Find the cells and give the type of each one.
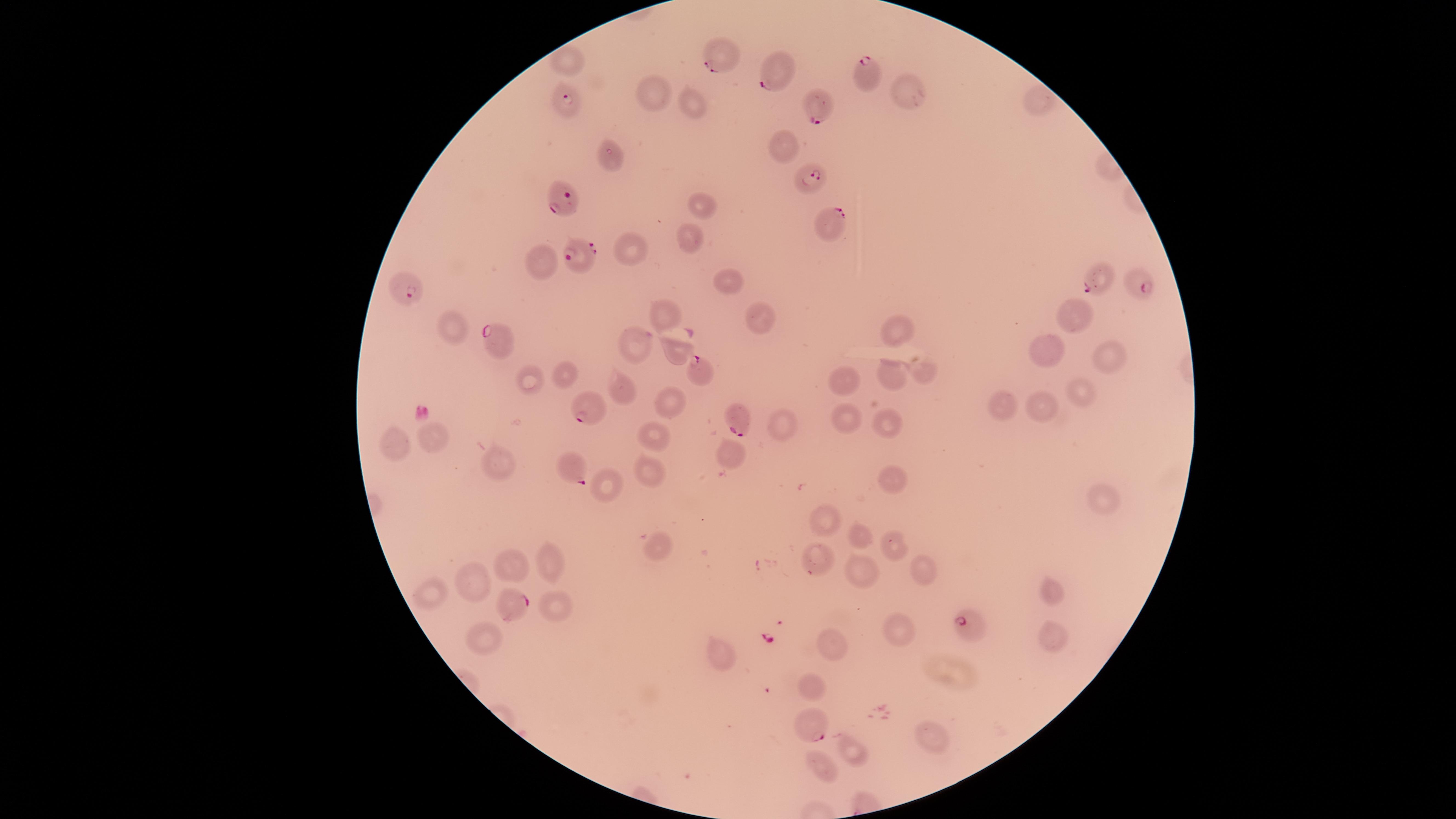
Approximate marker points, in pixels from the top-left corner.
Parasitized red blood cells: (x=719, y=62), (x=781, y=78), (x=861, y=78), (x=562, y=100), (x=820, y=109), (x=810, y=177), (x=560, y=203), (x=832, y=225), (x=576, y=262), (x=1093, y=277), (x=1135, y=285), (x=407, y=294), (x=500, y=342), (x=697, y=372), (x=589, y=407), (x=733, y=421), (x=573, y=470), (x=514, y=602), (x=966, y=625), (x=813, y=727).
Uninfected red blood cells: (x=566, y=60), (x=656, y=88), (x=906, y=89), (x=1037, y=98), (x=688, y=107), (x=784, y=145), (x=611, y=153), (x=699, y=207), (x=687, y=239), (x=630, y=243), (x=544, y=260), (x=724, y=280), (x=756, y=311), (x=669, y=313), (x=1076, y=314), (x=453, y=323), (x=897, y=329), (x=636, y=343), (x=1047, y=348), (x=673, y=350), (x=1111, y=359), (x=563, y=369), (x=926, y=369), (x=894, y=370), (x=846, y=376), (x=534, y=379), (x=621, y=390), (x=1079, y=390), (x=671, y=397), (x=989, y=404), (x=1038, y=408), (x=887, y=414), (x=843, y=416), (x=783, y=417), (x=653, y=435), (x=397, y=442), (x=430, y=444), (x=729, y=458), (x=500, y=462), (x=649, y=474), (x=888, y=482), (x=606, y=484), (x=1103, y=494), (x=826, y=524), (x=860, y=540), (x=892, y=544), (x=656, y=546), (x=818, y=556), (x=547, y=561), (x=507, y=564), (x=922, y=568), (x=864, y=571), (x=473, y=578), (x=1051, y=592), (x=435, y=595), (x=553, y=604), (x=900, y=626), (x=484, y=633), (x=1054, y=636), (x=830, y=646), (x=720, y=658), (x=812, y=684), (x=930, y=735), (x=845, y=753), (x=823, y=764).
No white blood cells identified.

{
  "stain": "Giemsa",
  "species": "Plasmodium falciparum",
  "image_size": "1456×819 pixels",
  "visible_region": "circular",
  "field_of_view": "single",
  "capture": "smartphone photograph through the microscope eyepiece",
  "preparation": "thin blood film"
}